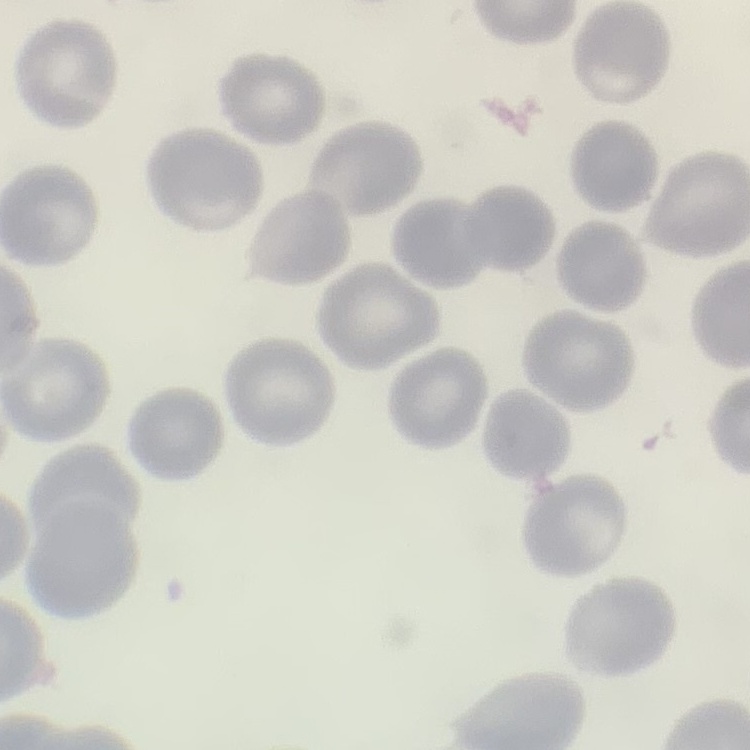
Summary:
  - Red blood cell morphology: no rouleaux formation
  - Preparation: thin blood film
  - Image type: one tile cut from a larger photomicrograph
  - Stain: Field's or Giemsa